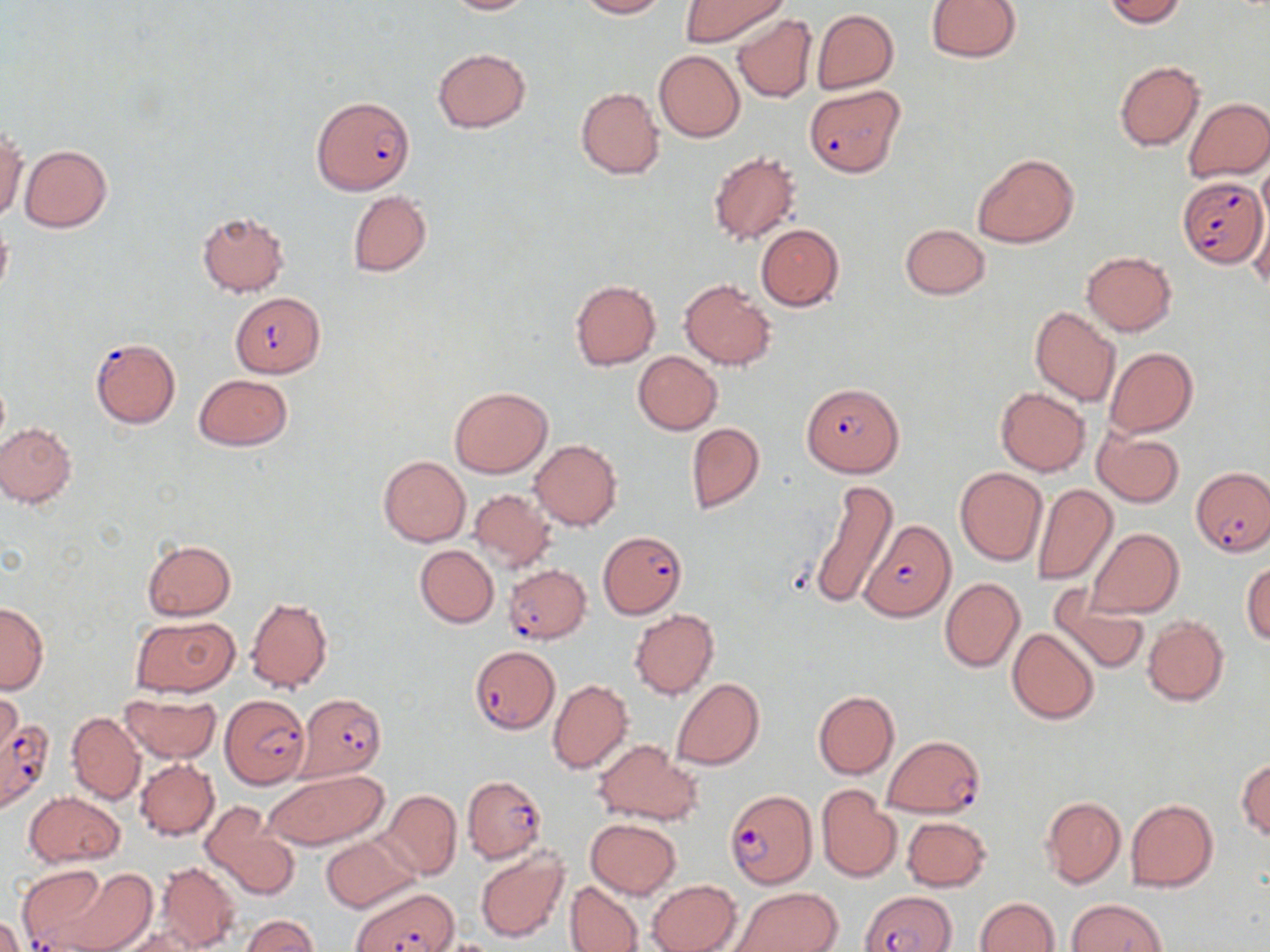

slide-level diagnosis = Plasmodium falciparum
preparation = thin blood smear
Plasmodium falciparum-infected red blood cell locations = approximate bounding boxes as (x1,y1)-(x2,y2) corner pairs in pixels: (804,85)-(903,176), (311,95)-(415,194), (1177,176)-(1268,268), (230,292)-(325,377), (90,337)-(181,428), (802,383)-(904,477), (1192,468)-(1270,555), (860,518)-(956,622), (600,529)-(687,620), (504,564)-(592,643), (469,644)-(560,733), (219,694)-(309,789), (298,694)-(387,780), (0,713)-(55,811), (883,736)-(986,817), (463,776)-(545,862), (724,788)-(818,888), (16,866)-(110,952), (353,884)-(458,952), (865,892)-(955,952)
stain = May-Grünwald-Giemsa
image size = 1270×952 pixels
uninfected red blood cell locations = approximate bounding boxes as (x1,y1)-(x2,y2) corner pairs in pixels: (441,0)-(531,14), (576,0)-(668,18), (681,0)-(787,47), (926,0)-(1022,63), (1104,0)-(1186,26), (812,9)-(899,94), (730,12)-(817,103), (432,48)-(531,133), (655,50)-(745,142), (1113,60)-(1205,152), (575,87)-(666,179), (1183,97)-(1270,183), (0,126)-(26,223), (20,145)-(113,232), (707,151)-(803,245), (971,152)-(1078,249), (1258,158)-(1270,233), (347,190)-(432,277), (1250,203)-(1270,291), (197,211)-(289,296), (0,217)-(12,302), (755,224)-(844,311), (899,224)-(991,300), (1081,251)-(1177,336), (678,278)-(777,370), (570,280)-(660,370), (1029,306)-(1122,407), (1104,346)-(1197,438), (632,352)-(723,435), (193,374)-(293,451), (450,387)-(553,478), (995,388)-(1091,476), (1,422)-(77,508), (685,422)-(765,514), (1093,430)-(1185,507), (530,439)-(622,530), (378,456)-(469,546), (955,467)-(1048,566), (807,480)-(897,609), (1032,483)-(1117,585), (469,488)-(553,571), (1087,529)-(1185,618), (141,540)-(235,621), (414,545)-(499,628), (1242,562)-(1270,645), (939,577)-(1024,672), (1051,588)-(1151,674), (1016,594)-(1139,710), (245,597)-(333,694), (0,603)-(48,693), (630,609)-(718,699), (128,616)-(240,697), (1142,617)-(1229,706), (1007,627)-(1099,724), (671,677)-(765,770), (548,679)-(633,774), (812,689)-(900,780), (120,693)-(221,763), (67,712)-(145,803), (592,739)-(700,825), (1236,758)-(1270,840), (135,759)-(219,840), (264,769)-(387,851), (816,784)-(902,882), (378,790)-(462,880), (24,791)-(125,867), (1041,796)-(1126,889), (1125,798)-(1219,892), (198,802)-(299,902), (902,816)-(992,892), (585,818)-(681,898), (322,835)-(416,912), (475,848)-(569,943), (155,862)-(242,951), (44,865)-(157,952), (645,879)-(741,952), (566,881)-(644,951), (728,887)-(842,952), (976,896)-(1059,951), (1067,898)-(1166,950), (243,915)-(318,952), (0,916)-(25,952), (110,924)-(207,952)
field of view = one of a larger specimen
modality = light microscopy
magnification = 1000x